State which parasite is depicted.
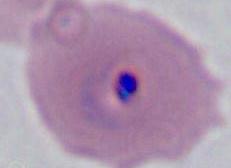

Plasmodium.

modality = photomicrograph
magnification = 400x or 1000x